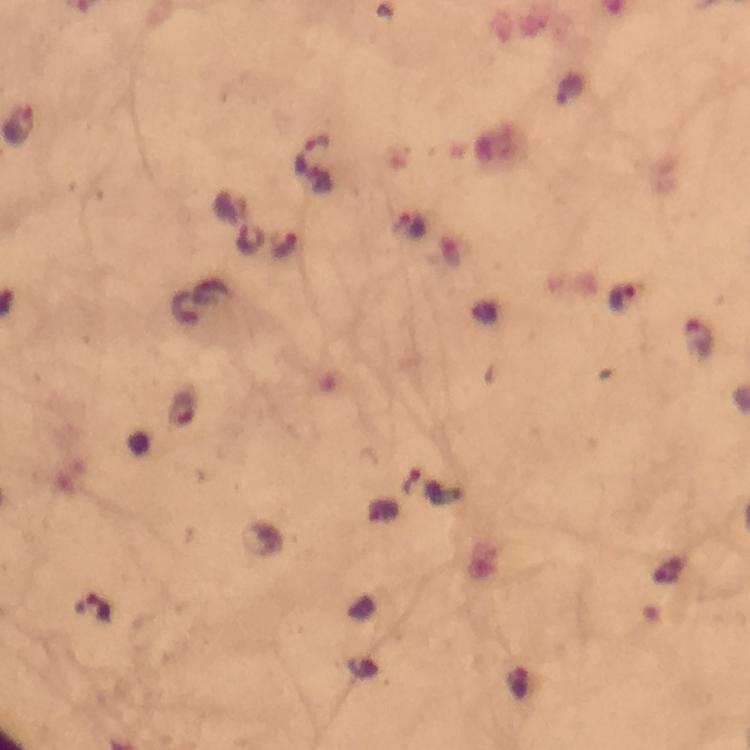 Approximate centers as {x, y} in pixels. Plasmodium parasite locations: {17, 125}, {312, 155}, {412, 226}, {283, 246}, {622, 297}, {699, 339}, {182, 411}, {94, 610}. Giemsa-stained preparation. Thick blood smear. Photographed with a smartphone mounted on the microscope. Image is 750×750 pixels. 100x magnification. From a malaria diagnostic workup. Cropped region of a single field of view. Immersion oil was used.